Locate every P. falciparum parasite and give its life-cycle stage, and locate every leukocyte and any debris.
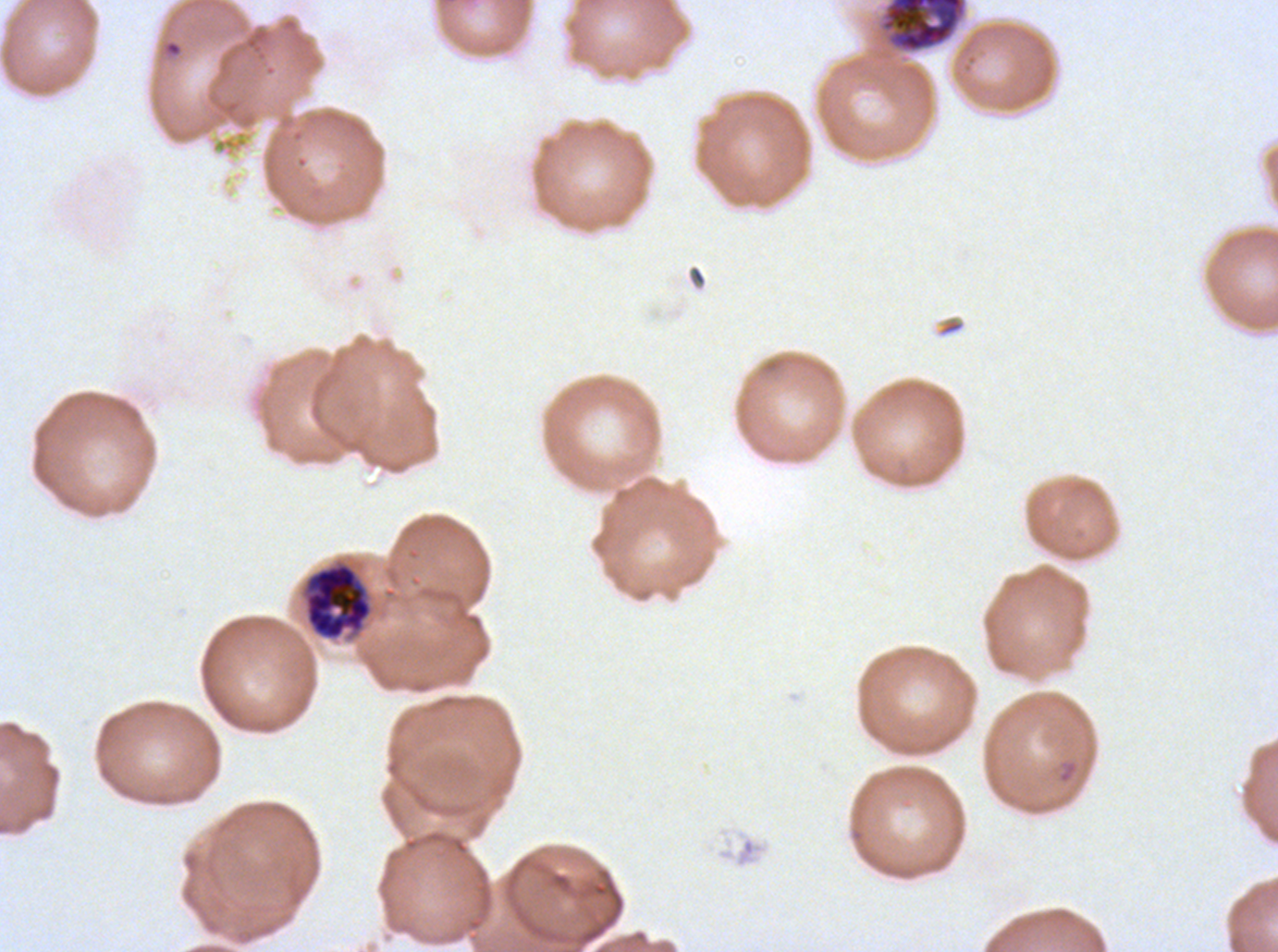

Approximate bounding boxes as (x1, y1, x2, y2) in pixels.
Rings: (164, 40, 183, 57).
Late schizonts: (878, 0, 968, 55), (303, 562, 373, 641).
No late-ring/early-trophozoite forms, mid trophozoites, late trophozoites, early schizonts, segmenters, gametocytes, leukocytes, or debris observed.

Summary:
  - Stain: Giemsa
  - Preparation: thin blood smear
  - Image size: 1278×952 pixels
  - Life-cycle stages observed: ring, late schizont
  - Specimen: P. falciparum cultured ex vivo for 24 to 48 hours, from a patient in The Gambia
  - Field of view: sub-image separated from a larger composite